Name the cell type shown.
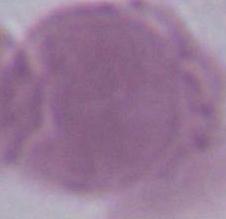
An erythrocyte.

Summary:
  - Magnification: 1000x
  - Modality: photomicrograph